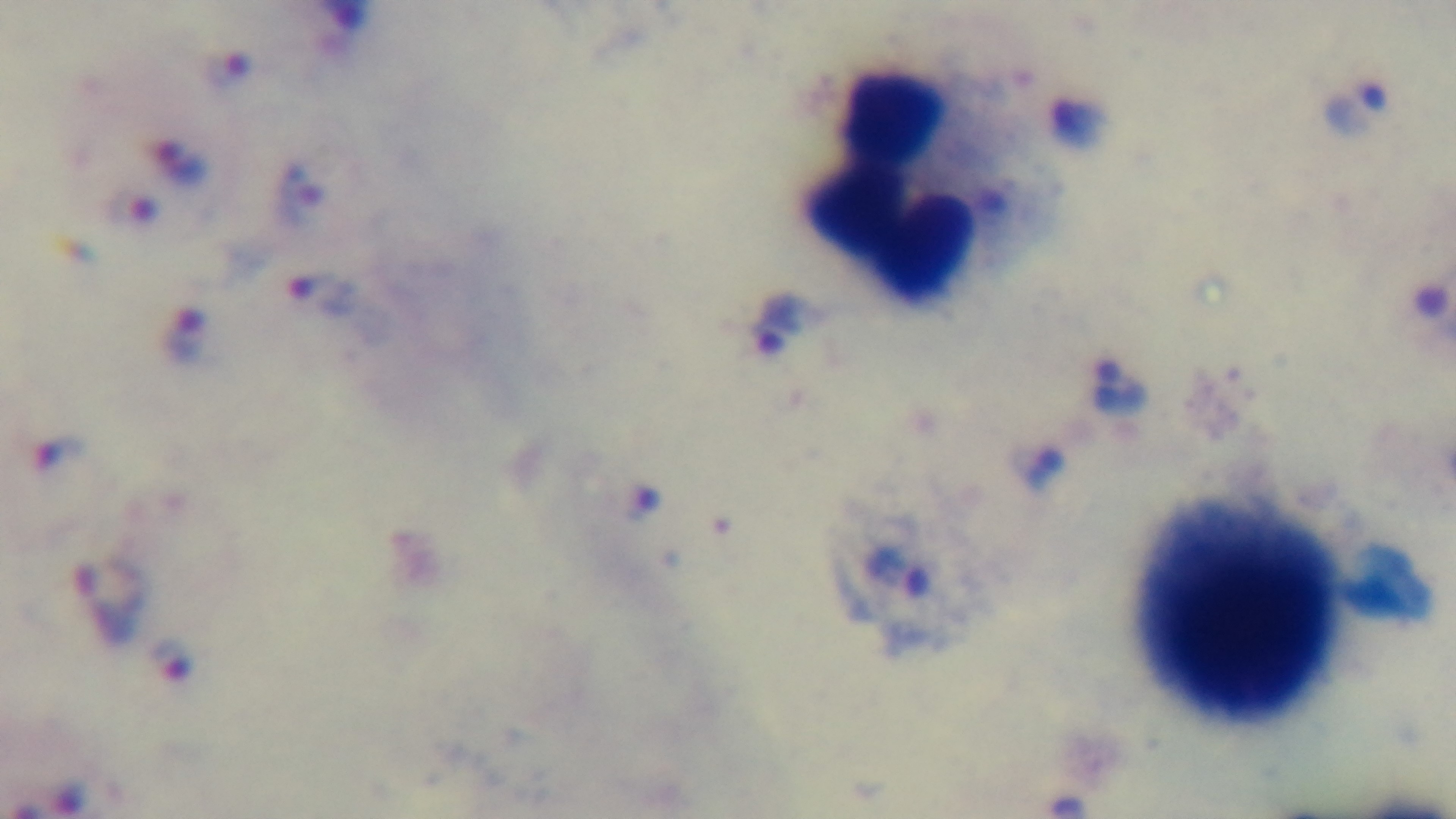
preparation = thick blood film
capture = mounted 4K digital camera
modality = light microscopy
field of view = single
objective = 100x oil immersion
stain = Giemsa
malaria status = infected